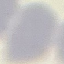

malaria_status: uninfected
preparation: thin blood smear
capture: smartphone camera at the microscope eyepiece
image_type: cell patch, automatically extracted from a larger field of view and resized to 64 × 64 pixels
stain: Giemsa